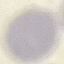
Malaria status: uninfected. Giemsa-stained preparation. Photographed with a smartphone camera at the microscope eyepiece. Automatically extracted cell patch, resized to 64 × 64 pixels. Thin blood film.